Outline each Trypanosoma brucei.
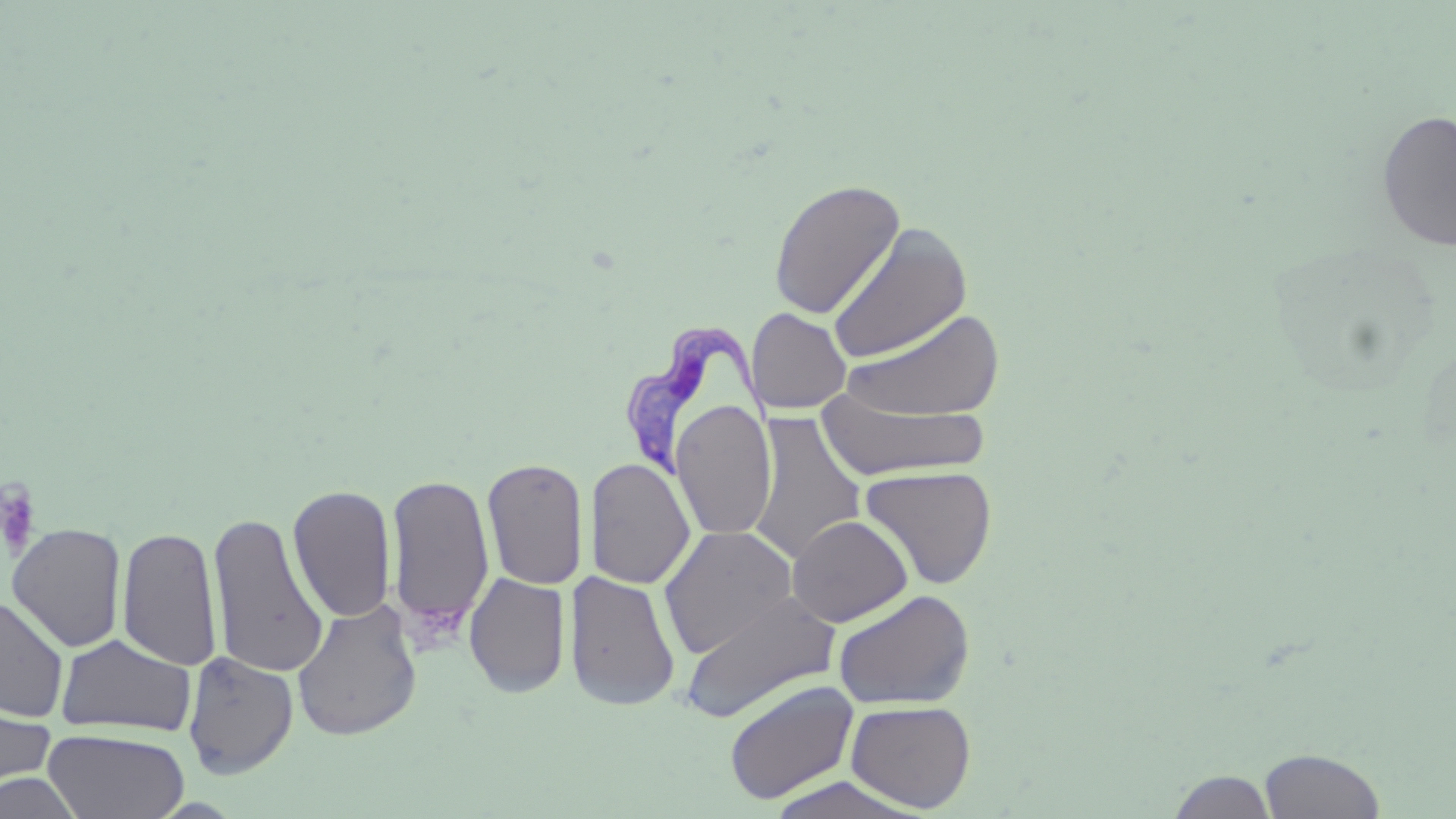

Approximate bounding boxes as [x1, y1, x2, y2] in pixels.
Trypanosoma brucei: [624, 321, 778, 477].

Platelet locations: [0, 482, 42, 560]. Uninfected red blood cell locations: [1376, 109, 1456, 253], [768, 178, 906, 320], [827, 223, 973, 366], [839, 307, 1005, 423], [746, 308, 852, 415], [817, 391, 992, 480], [671, 400, 777, 541], [748, 411, 867, 565], [482, 457, 588, 590], [585, 457, 695, 591], [859, 464, 998, 590], [387, 472, 495, 641], [288, 484, 397, 623], [207, 510, 329, 679], [787, 515, 913, 627], [7, 523, 127, 652], [117, 523, 223, 672], [658, 524, 798, 657], [566, 570, 681, 713], [464, 571, 570, 698], [832, 589, 976, 710], [678, 591, 842, 724], [0, 594, 70, 722], [292, 598, 422, 742], [55, 634, 196, 738], [182, 651, 298, 779], [724, 680, 858, 804], [0, 691, 57, 803], [845, 700, 977, 812], [43, 728, 190, 819], [1258, 747, 1386, 818], [1168, 770, 1278, 818], [0, 771, 84, 818], [764, 773, 929, 818]. Slide-level diagnosis: Trypanosoma brucei. May-Grünwald-Giemsa-stained preparation. Image is 1456×819 pixels. Single field of view. Light microscopy. Thin blood film. Captured at 1000x magnification.